Outline each blood parasite and name the species.
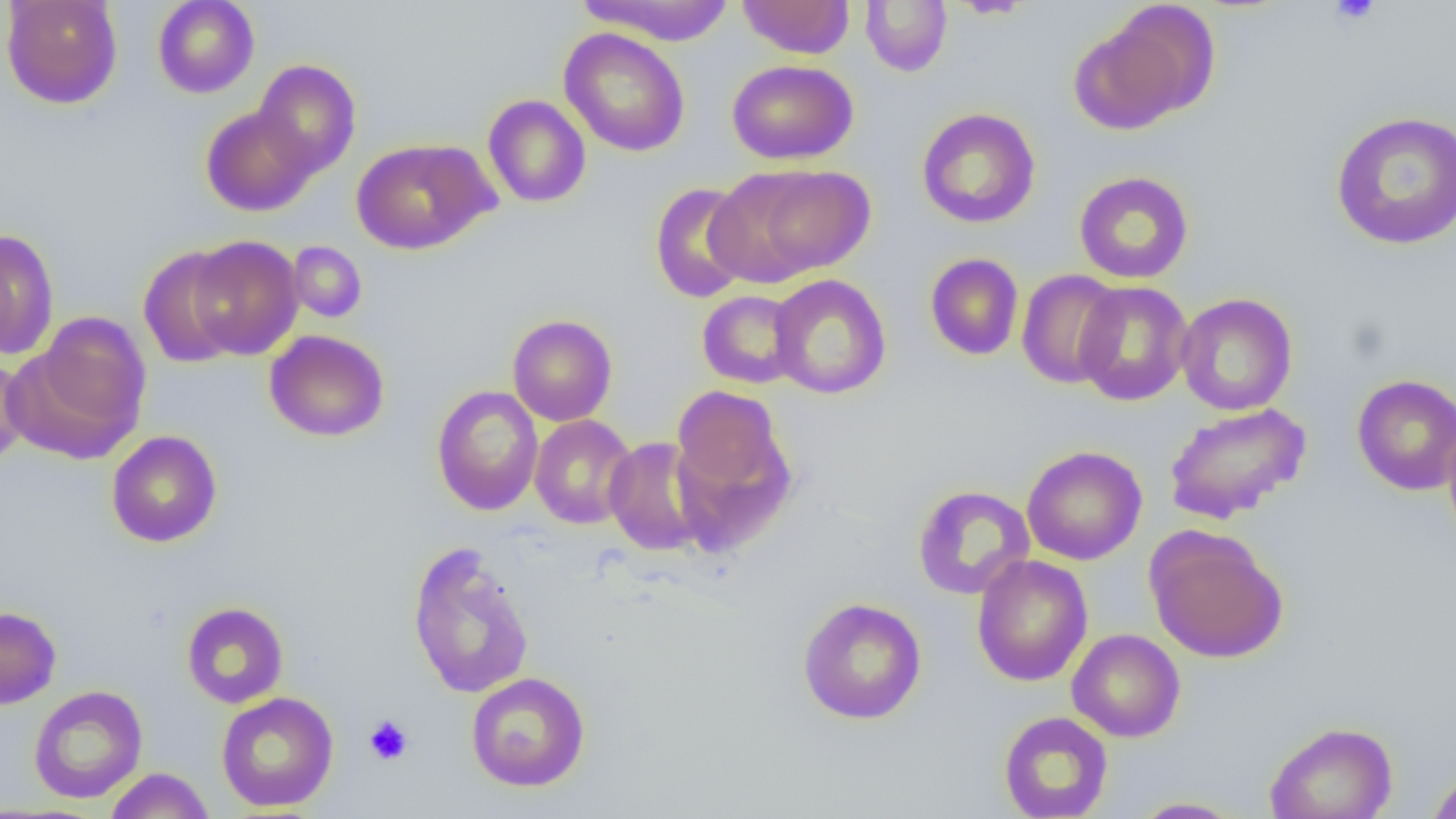

No blood parasites observed.

slide-level diagnosis = negative for blood parasites
uninfected red blood cell locations = approximate bounding boxes as (x1,y1)-(x2,y2) corner pairs in pixels: (1,0)-(123,109), (152,0)-(259,98), (577,0)-(736,45), (738,0)-(854,59), (859,1)-(952,76), (1075,5)-(1217,132), (559,27)-(690,157), (252,59)-(361,177), (727,59)-(858,165), (482,94)-(591,208), (200,105)-(317,216), (916,107)-(1041,228), (1330,111)-(1456,250), (351,138)-(493,254), (749,165)-(876,276), (1073,171)-(1194,284), (648,174)-(864,292), (649,181)-(756,304), (0,229)-(59,361), (184,235)-(304,360), (287,241)-(367,323), (138,247)-(245,368), (924,253)-(1024,361), (1016,269)-(1125,389), (769,274)-(891,399), (1073,280)-(1194,406), (697,290)-(805,389), (1176,292)-(1298,416), (12,313)-(151,458), (507,314)-(618,426), (264,329)-(390,442), (0,353)-(30,468), (1352,374)-(1456,495), (669,384)-(793,513), (431,385)-(544,515), (1164,402)-(1311,525), (529,414)-(638,529), (1442,418)-(1456,545), (105,430)-(222,548), (603,437)-(708,556), (1022,445)-(1147,565), (912,484)-(1036,600), (1143,525)-(1289,663), (407,541)-(535,699), (971,555)-(1093,686), (797,597)-(927,724), (181,602)-(289,708), (0,606)-(61,709), (1067,629)-(1185,742), (465,671)-(591,792), (28,685)-(148,803), (216,691)-(338,812), (998,711)-(1113,818), (1265,721)-(1398,819), (104,767)-(214,819), (1427,767)-(1456,819), (1129,797)-(1249,818)
field of view = single
magnification = 1000x
platelet locations = approximate bounding boxes as (x1,y1)-(x2,y2) corner pairs in pixels: (1329,0)-(1381,25), (363,715)-(413,765)
preparation = thin blood smear
modality = light microscopy
image size = 1456×819 pixels